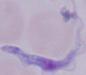

magnification = 1000x
identification = trypanosome
modality = photomicrograph